Classify this cell by malaria status.
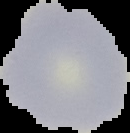
Uninfected.

From a thin blood film. Image is 130×133 pixels. The area outside the segmented cell region is set to black.